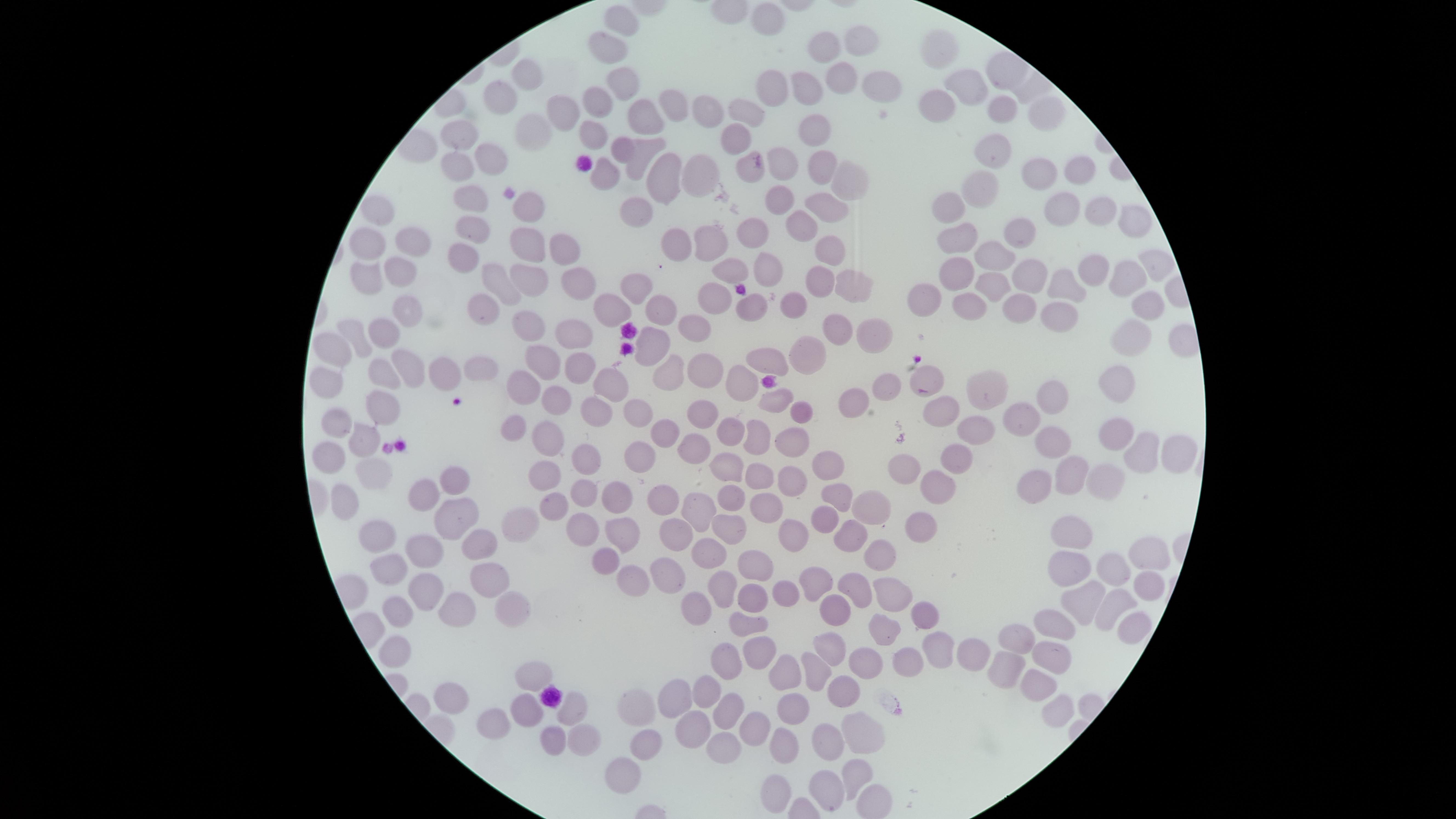
Approximate marker points, in pixels from the top-left corner.
Summary:
  - Uninfected red blood cells: (x=762, y=12), (x=624, y=21), (x=858, y=37), (x=609, y=47), (x=941, y=47), (x=819, y=53), (x=529, y=73), (x=964, y=80), (x=624, y=83), (x=835, y=83), (x=876, y=86), (x=767, y=89), (x=802, y=90), (x=503, y=94), (x=935, y=101), (x=674, y=102), (x=597, y=103), (x=1007, y=106), (x=561, y=111), (x=707, y=111), (x=747, y=111), (x=1042, y=112), (x=641, y=116), (x=463, y=128), (x=526, y=128), (x=592, y=128), (x=811, y=132), (x=736, y=134), (x=619, y=149), (x=993, y=150), (x=491, y=151), (x=636, y=151), (x=455, y=163), (x=819, y=164), (x=697, y=166), (x=751, y=166), (x=782, y=166), (x=1076, y=168), (x=662, y=171), (x=1037, y=171), (x=841, y=175), (x=602, y=176), (x=987, y=182), (x=472, y=197), (x=780, y=197), (x=953, y=198), (x=527, y=199), (x=822, y=204), (x=638, y=206), (x=378, y=208), (x=1058, y=208), (x=1097, y=209), (x=1127, y=216), (x=797, y=222), (x=1014, y=227), (x=478, y=229), (x=751, y=231), (x=954, y=234), (x=411, y=239), (x=707, y=239), (x=369, y=242), (x=528, y=242), (x=676, y=244), (x=824, y=247), (x=463, y=251), (x=996, y=252), (x=554, y=253), (x=1156, y=261), (x=769, y=264), (x=1090, y=264), (x=399, y=266), (x=736, y=267), (x=954, y=271), (x=365, y=274), (x=1026, y=275), (x=817, y=276), (x=534, y=277), (x=573, y=277), (x=845, y=280), (x=508, y=282), (x=1064, y=282), (x=1123, y=282), (x=635, y=285), (x=984, y=288), (x=929, y=294), (x=714, y=295), (x=662, y=302), (x=966, y=303), (x=1017, y=303), (x=1143, y=303), (x=750, y=305), (x=792, y=305), (x=406, y=308), (x=613, y=308), (x=484, y=311), (x=1058, y=312), (x=527, y=329), (x=573, y=329), (x=695, y=329), (x=869, y=329), (x=829, y=330), (x=385, y=333), (x=1134, y=334), (x=653, y=340), (x=360, y=341), (x=336, y=344), (x=808, y=356), (x=767, y=357), (x=537, y=363), (x=483, y=364), (x=405, y=366), (x=579, y=366), (x=710, y=368), (x=447, y=373), (x=664, y=374), (x=379, y=375), (x=742, y=377), (x=326, y=378), (x=933, y=379), (x=607, y=381), (x=883, y=384), (x=1109, y=385), (x=519, y=386), (x=988, y=388), (x=1055, y=390), (x=548, y=392), (x=855, y=396), (x=776, y=397), (x=378, y=405), (x=599, y=408), (x=804, y=409), (x=1017, y=410), (x=638, y=412), (x=706, y=412), (x=942, y=412), (x=335, y=422), (x=520, y=425), (x=967, y=428), (x=665, y=429), (x=733, y=430), (x=753, y=433), (x=784, y=434), (x=360, y=436), (x=555, y=436), (x=1118, y=438), (x=1056, y=442), (x=697, y=448), (x=957, y=452), (x=1174, y=453), (x=1145, y=454), (x=329, y=455), (x=642, y=455), (x=584, y=460), (x=729, y=464), (x=829, y=464), (x=906, y=464), (x=369, y=470), (x=544, y=471), (x=762, y=472), (x=1069, y=475), (x=454, y=478), (x=792, y=478), (x=1107, y=478), (x=943, y=481), (x=1036, y=487), (x=583, y=489), (x=614, y=489), (x=426, y=491), (x=732, y=491), (x=839, y=491), (x=345, y=495), (x=661, y=500), (x=548, y=505), (x=769, y=506), (x=875, y=506), (x=700, y=510), (x=458, y=515), (x=820, y=520), (x=585, y=522), (x=522, y=523), (x=919, y=524), (x=622, y=526), (x=729, y=527), (x=675, y=532), (x=855, y=532), (x=1078, y=532), (x=790, y=535), (x=377, y=536), (x=479, y=538), (x=426, y=549), (x=1145, y=551), (x=601, y=552), (x=707, y=552), (x=880, y=552), (x=758, y=564), (x=1071, y=567), (x=665, y=569), (x=1116, y=571), (x=485, y=572), (x=393, y=574), (x=627, y=576), (x=811, y=579), (x=856, y=581), (x=1147, y=582), (x=719, y=588), (x=424, y=590), (x=889, y=590), (x=784, y=591), (x=754, y=594), (x=505, y=597), (x=1085, y=600), (x=689, y=601), (x=832, y=604), (x=929, y=608), (x=443, y=609), (x=1107, y=609), (x=395, y=611), (x=749, y=623), (x=1055, y=623), (x=884, y=625), (x=1139, y=626), (x=835, y=643), (x=1017, y=643), (x=755, y=644), (x=938, y=648), (x=980, y=651), (x=392, y=653), (x=731, y=657), (x=862, y=657), (x=1054, y=657), (x=908, y=659), (x=1006, y=660), (x=814, y=666), (x=784, y=670), (x=528, y=676), (x=1038, y=684), (x=708, y=686), (x=842, y=692), (x=681, y=696), (x=453, y=697), (x=797, y=698), (x=566, y=706), (x=1052, y=706), (x=521, y=707), (x=725, y=707), (x=639, y=709), (x=493, y=721), (x=689, y=723), (x=750, y=725), (x=856, y=735), (x=784, y=739), (x=547, y=740), (x=580, y=740), (x=828, y=741), (x=644, y=746), (x=720, y=746), (x=622, y=768), (x=853, y=773), (x=777, y=785), (x=828, y=790)
  - Capture: smartphone photograph through the microscope eyepiece
  - Image size: 1456×819 pixels
  - Stain: Giemsa
  - Visible region: circular
  - Field of view: single
  - Preparation: thin blood film
  - Presence: no malaria parasites identified